Identify the blood parasite species.
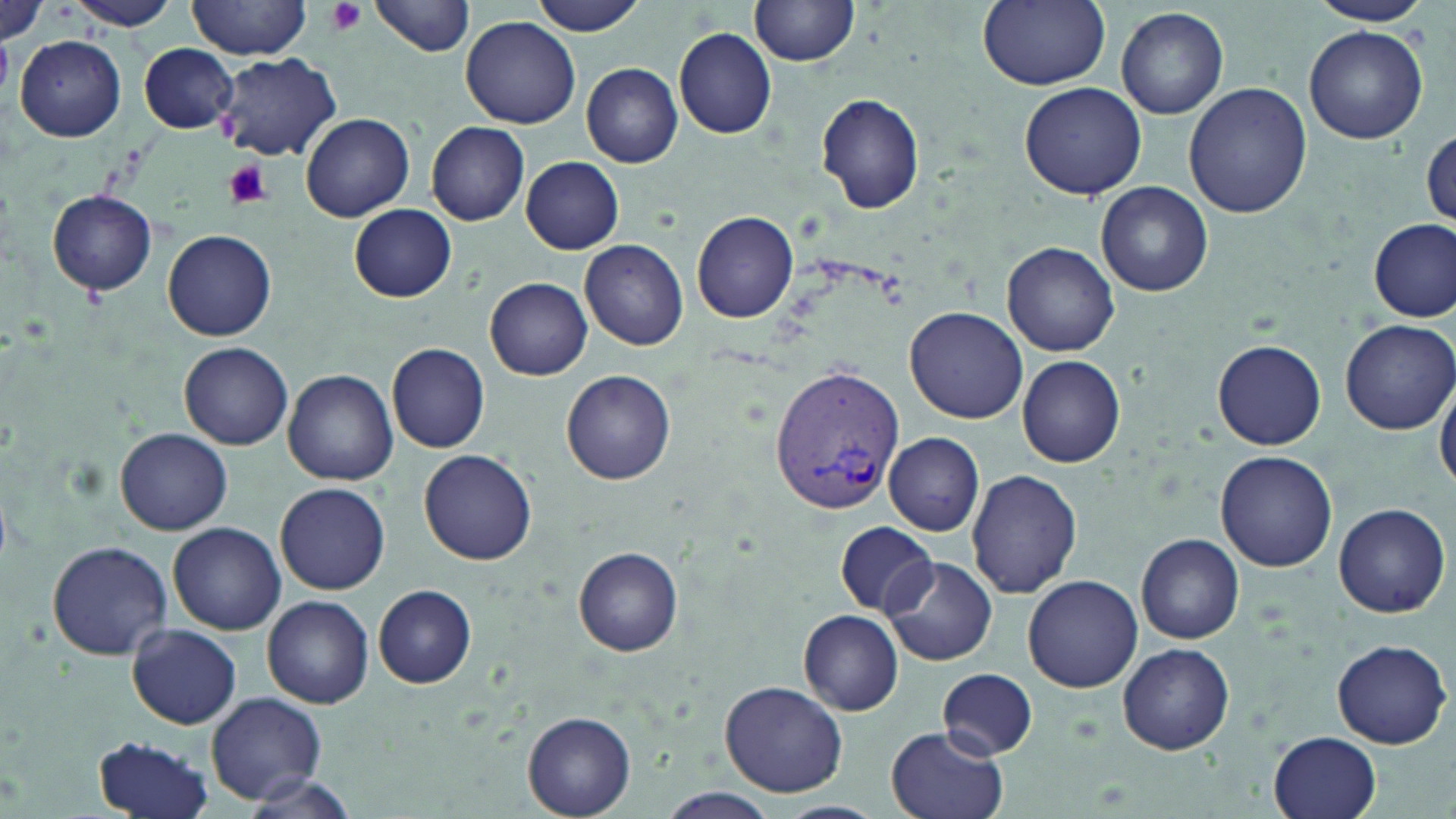

Plasmodium vivax.

Summary:
  - Coordinate format: approximate bounding boxes as named x1/y1/x2/y2 corners in pixels
  - Plasmodium vivax-infected red blood cell locations: (x1=768, y1=364, x2=902, y2=518)
  - Uninfected red blood cell locations: (x1=68, y1=0, x2=181, y2=31), (x1=188, y1=0, x2=310, y2=59), (x1=371, y1=0, x2=477, y2=56), (x1=534, y1=0, x2=648, y2=35), (x1=976, y1=0, x2=1110, y2=89), (x1=1306, y1=0, x2=1434, y2=27), (x1=0, y1=1, x2=52, y2=47), (x1=752, y1=2, x2=860, y2=67), (x1=1116, y1=6, x2=1228, y2=119), (x1=460, y1=15, x2=582, y2=129), (x1=1305, y1=25, x2=1427, y2=144), (x1=674, y1=27, x2=776, y2=138), (x1=15, y1=35, x2=126, y2=142), (x1=138, y1=43, x2=240, y2=133), (x1=214, y1=53, x2=340, y2=161), (x1=580, y1=62, x2=683, y2=167), (x1=1183, y1=81, x2=1313, y2=218), (x1=1019, y1=83, x2=1149, y2=200), (x1=816, y1=93, x2=925, y2=214), (x1=302, y1=112, x2=416, y2=221), (x1=426, y1=122, x2=530, y2=226), (x1=1421, y1=125, x2=1455, y2=233), (x1=520, y1=156, x2=625, y2=254), (x1=1096, y1=182, x2=1211, y2=295), (x1=48, y1=189, x2=158, y2=295), (x1=350, y1=204, x2=457, y2=303), (x1=692, y1=212, x2=798, y2=322), (x1=1368, y1=218, x2=1454, y2=321), (x1=164, y1=230, x2=276, y2=341), (x1=580, y1=240, x2=689, y2=350), (x1=1003, y1=241, x2=1119, y2=356), (x1=485, y1=277, x2=593, y2=380), (x1=906, y1=306, x2=1029, y2=425), (x1=1340, y1=319, x2=1456, y2=434), (x1=1214, y1=340, x2=1325, y2=449), (x1=180, y1=342, x2=293, y2=450), (x1=388, y1=343, x2=491, y2=454), (x1=1018, y1=355, x2=1125, y2=468), (x1=283, y1=369, x2=397, y2=485), (x1=562, y1=369, x2=677, y2=484), (x1=1436, y1=371, x2=1456, y2=492), (x1=115, y1=428, x2=233, y2=535), (x1=884, y1=431, x2=985, y2=535), (x1=419, y1=450, x2=538, y2=566), (x1=1215, y1=451, x2=1340, y2=573), (x1=967, y1=469, x2=1083, y2=598), (x1=275, y1=482, x2=390, y2=594), (x1=1332, y1=502, x2=1451, y2=617), (x1=835, y1=520, x2=939, y2=616), (x1=168, y1=522, x2=287, y2=635), (x1=1136, y1=534, x2=1245, y2=644), (x1=46, y1=540, x2=172, y2=660), (x1=574, y1=546, x2=685, y2=656), (x1=881, y1=555, x2=998, y2=667), (x1=1022, y1=574, x2=1143, y2=693), (x1=373, y1=584, x2=477, y2=689), (x1=262, y1=596, x2=374, y2=708), (x1=798, y1=610, x2=904, y2=716), (x1=126, y1=623, x2=242, y2=730), (x1=1331, y1=638, x2=1451, y2=749), (x1=1117, y1=643, x2=1235, y2=754), (x1=938, y1=668, x2=1038, y2=758), (x1=721, y1=680, x2=847, y2=797), (x1=206, y1=691, x2=326, y2=806), (x1=523, y1=712, x2=635, y2=817), (x1=886, y1=725, x2=1012, y2=819), (x1=1269, y1=732, x2=1382, y2=819), (x1=91, y1=735, x2=218, y2=819), (x1=237, y1=774, x2=361, y2=818)
  - Platelet locations: (x1=324, y1=0, x2=366, y2=35), (x1=225, y1=161, x2=273, y2=209)
  - Stain: May-Grünwald-Giemsa
  - Magnification: 1000x
  - Modality: light microscopy
  - Image size: 1456×819 pixels
  - Field of view: single
  - Preparation: thin blood smear